Classify this cell by malaria status.
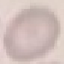
It is uninfected.

Automatically extracted cell patch, resized to 64 × 64 pixels. Photographed with a smartphone camera at the microscope eyepiece. Thin smear of blood. Giemsa-stained preparation.